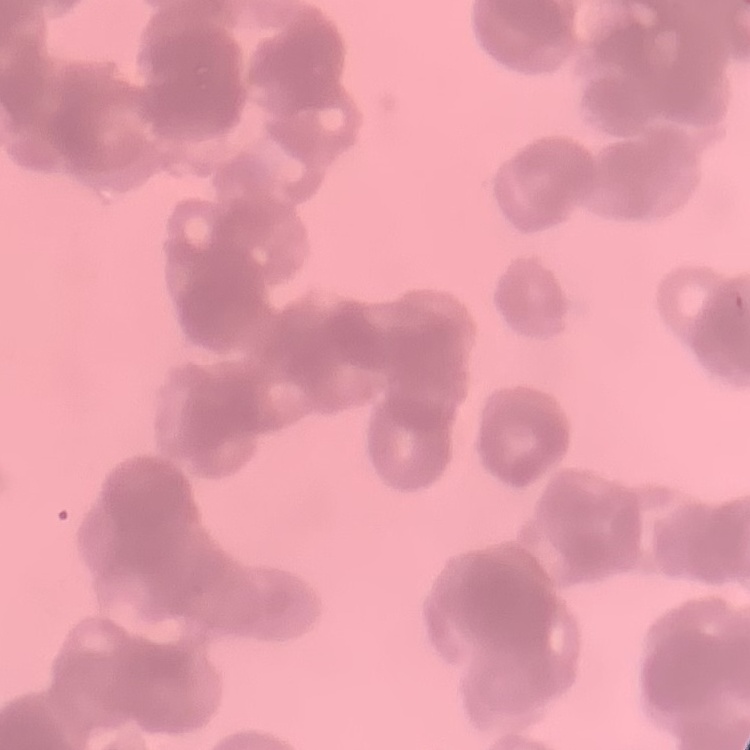
Summary:
  - Red blood cell morphology: rouleaux formation
  - Preparation: thin blood smear
  - Stain: Field's or Giemsa
  - Image type: one tile cut from a larger photomicrograph